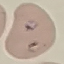

Result: malaria parasites detected. Automatically extracted cell patch, resized to 64 × 64 pixels. Giemsa stain. Thin smear of blood. Photographed with a smartphone camera at the microscope eyepiece.